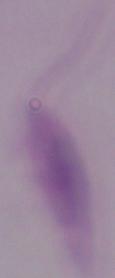

Summary:
  - Magnification: 1000x
  - Modality: micrograph
  - Identification: Leishmania